Evaluate for Plasmodium parasites.
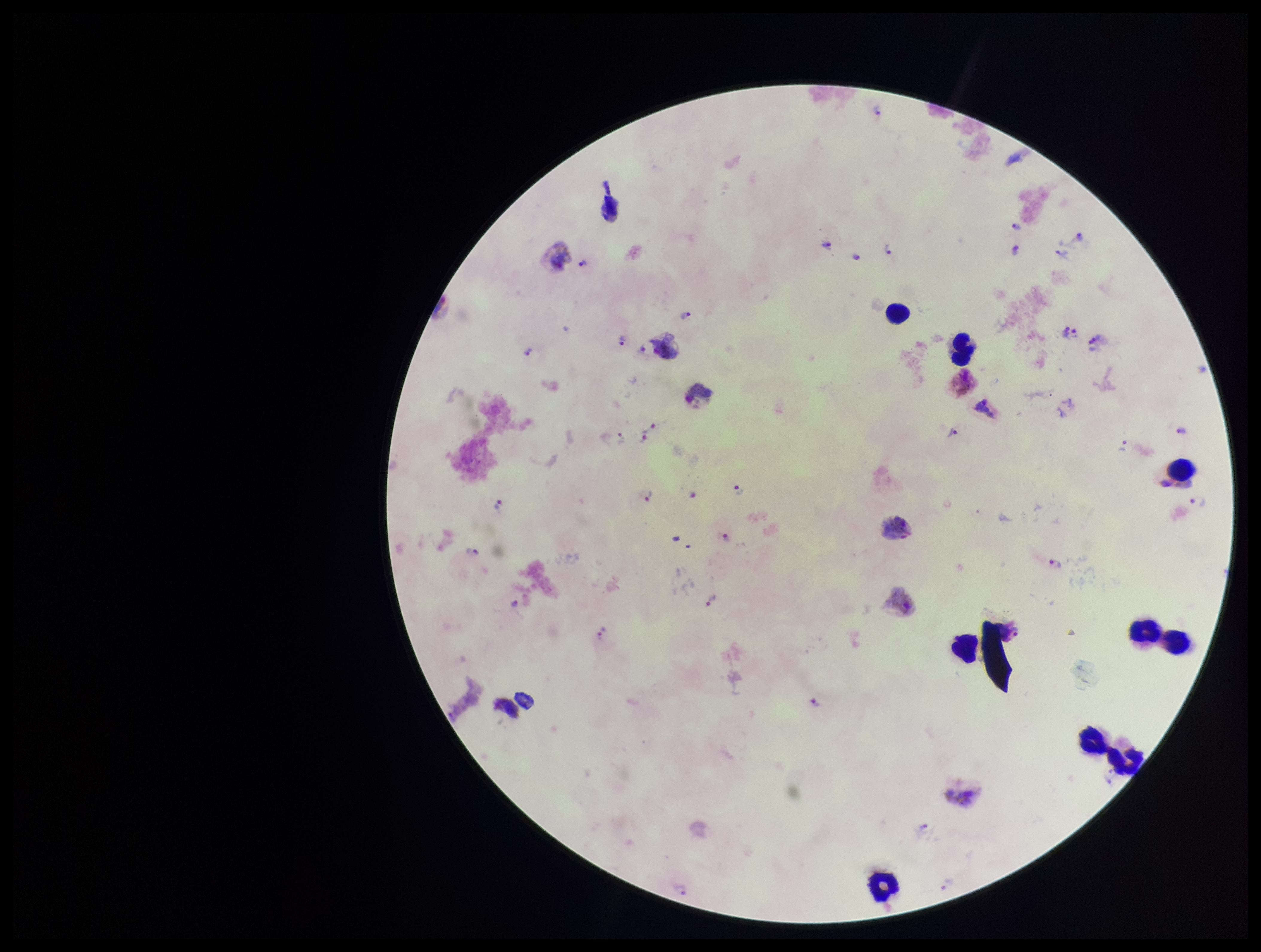

Seen.

Leukocyte count: 9. Stained with Giemsa. Parasite count: 31. Preparation: thick. Patient malaria status: infected. Image is 1261×952 pixels. Smartphone photograph taken through the eyepiece of a microscope. Species reported for this patient: Plasmodium vivax. One field from this slide.